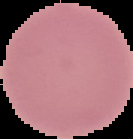
Cell region segmented out of the field of view; the surrounding area is masked to black. Malaria status: uninfected. From a thin blood smear. Image is 133×139 pixels.